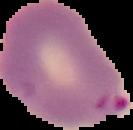 The area outside the segmented cell region is set to black. From a thin blood smear. Image is 133×130 pixels. Malaria status: parasitized.